Assess this cell for malaria.
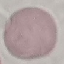

It is uninfected.

stain: Giemsa
preparation: thin smear
image_type: automatically extracted cell patch, resized to 64 × 64 pixels
capture: smartphone through the microscope eyepiece